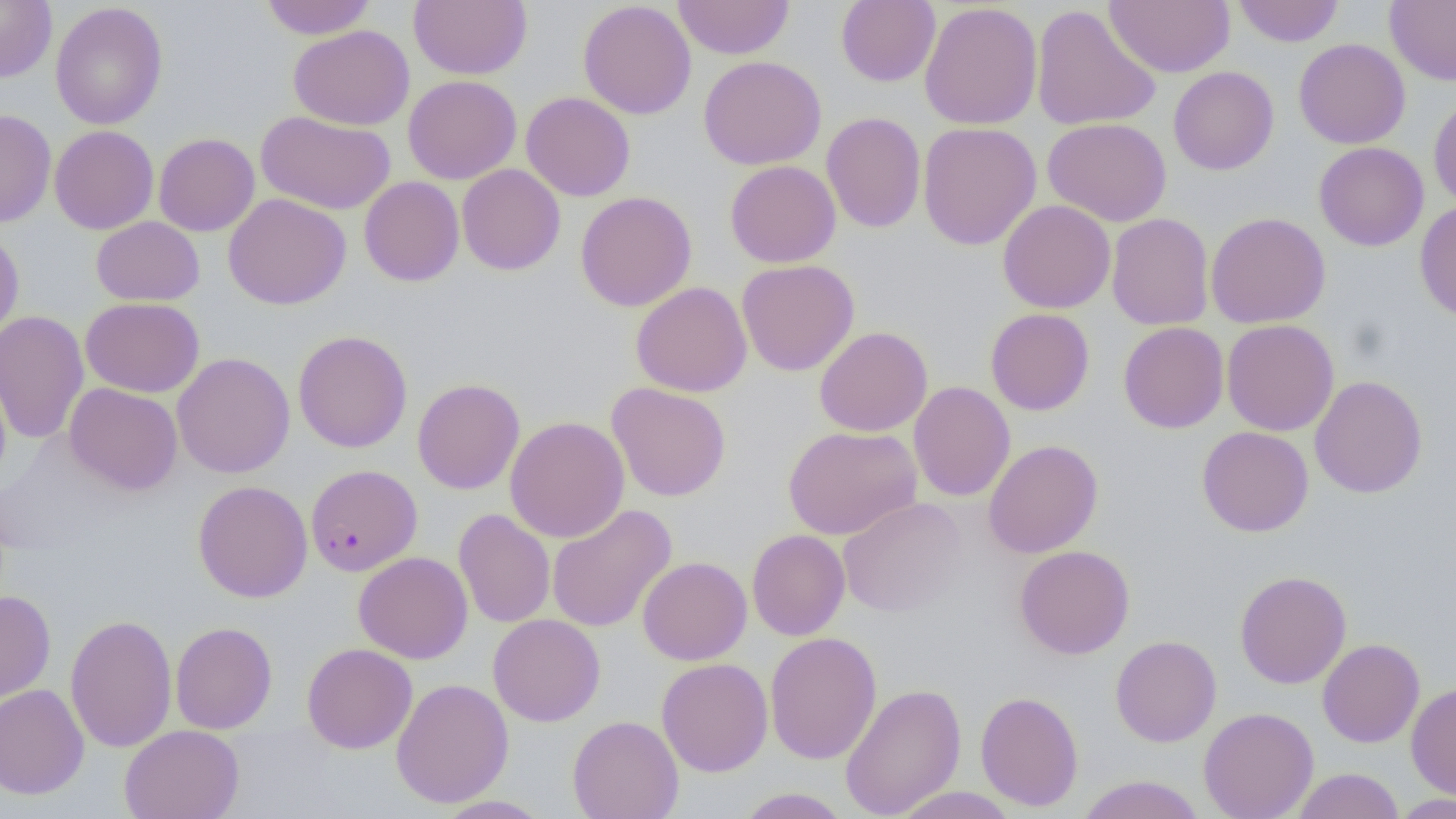
{
  "slide_level_diagnosis": "Plasmodium falciparum",
  "magnification": "1000x",
  "uninfected_red_blood_cell_locations": "approximate bounding boxes as named x1/y1/x2/y2 corners in pixels: (x1=0, y1=0, x2=56, y2=82), (x1=259, y1=0, x2=377, y2=39), (x1=409, y1=0, x2=532, y2=80), (x1=578, y1=0, x2=697, y2=119), (x1=672, y1=0, x2=794, y2=59), (x1=836, y1=0, x2=941, y2=87), (x1=1104, y1=0, x2=1234, y2=77), (x1=1233, y1=0, x2=1344, y2=47), (x1=1385, y1=0, x2=1456, y2=85), (x1=919, y1=1, x2=1042, y2=130), (x1=50, y1=2, x2=167, y2=130), (x1=1031, y1=4, x2=1161, y2=131), (x1=289, y1=25, x2=414, y2=130), (x1=1294, y1=38, x2=1410, y2=148), (x1=698, y1=55, x2=826, y2=170), (x1=1168, y1=66, x2=1279, y2=175), (x1=403, y1=75, x2=522, y2=184), (x1=521, y1=92, x2=636, y2=201), (x1=1429, y1=95, x2=1456, y2=210), (x1=0, y1=109, x2=56, y2=227), (x1=256, y1=111, x2=396, y2=214), (x1=822, y1=112, x2=925, y2=232), (x1=1043, y1=117, x2=1172, y2=226), (x1=918, y1=121, x2=1042, y2=250), (x1=50, y1=125, x2=158, y2=234), (x1=154, y1=133, x2=260, y2=236), (x1=1314, y1=142, x2=1429, y2=251), (x1=725, y1=160, x2=841, y2=268), (x1=457, y1=164, x2=565, y2=276), (x1=359, y1=176, x2=464, y2=287), (x1=575, y1=191, x2=696, y2=312), (x1=223, y1=193, x2=351, y2=309), (x1=997, y1=200, x2=1116, y2=313), (x1=1415, y1=201, x2=1456, y2=322), (x1=1107, y1=212, x2=1213, y2=331), (x1=1206, y1=212, x2=1330, y2=329), (x1=91, y1=216, x2=205, y2=306), (x1=0, y1=230, x2=24, y2=344), (x1=737, y1=259, x2=859, y2=376), (x1=630, y1=281, x2=752, y2=397), (x1=81, y1=298, x2=204, y2=397), (x1=985, y1=308, x2=1095, y2=415), (x1=0, y1=310, x2=89, y2=445), (x1=1222, y1=319, x2=1339, y2=436), (x1=1118, y1=321, x2=1229, y2=433), (x1=814, y1=326, x2=932, y2=437), (x1=292, y1=330, x2=413, y2=453), (x1=172, y1=352, x2=294, y2=478), (x1=1310, y1=375, x2=1428, y2=498), (x1=412, y1=377, x2=525, y2=495), (x1=909, y1=381, x2=1015, y2=501), (x1=606, y1=382, x2=731, y2=501), (x1=64, y1=383, x2=183, y2=495), (x1=504, y1=416, x2=630, y2=543), (x1=783, y1=425, x2=922, y2=539), (x1=1197, y1=426, x2=1313, y2=537), (x1=984, y1=439, x2=1103, y2=558), (x1=193, y1=480, x2=312, y2=603), (x1=838, y1=497, x2=968, y2=617), (x1=547, y1=504, x2=677, y2=633), (x1=453, y1=508, x2=555, y2=628), (x1=747, y1=529, x2=850, y2=640), (x1=1014, y1=545, x2=1135, y2=659), (x1=353, y1=551, x2=473, y2=663), (x1=637, y1=556, x2=752, y2=665), (x1=1235, y1=569, x2=1352, y2=689), (x1=0, y1=591, x2=56, y2=703), (x1=65, y1=613, x2=177, y2=754), (x1=488, y1=614, x2=605, y2=726), (x1=170, y1=622, x2=277, y2=734), (x1=764, y1=631, x2=882, y2=764), (x1=1110, y1=635, x2=1222, y2=747), (x1=1317, y1=638, x2=1425, y2=747), (x1=302, y1=643, x2=417, y2=753), (x1=657, y1=658, x2=773, y2=776), (x1=391, y1=677, x2=513, y2=808), (x1=840, y1=682, x2=966, y2=819), (x1=1406, y1=682, x2=1456, y2=800), (x1=0, y1=683, x2=89, y2=799), (x1=975, y1=690, x2=1084, y2=811), (x1=1198, y1=707, x2=1319, y2=819), (x1=567, y1=715, x2=684, y2=819), (x1=120, y1=724, x2=244, y2=819), (x1=1292, y1=768, x2=1404, y2=819), (x1=1075, y1=775, x2=1206, y2=819), (x1=889, y1=786, x2=1019, y2=818), (x1=734, y1=787, x2=853, y2=818), (x1=1390, y1=793, x2=1455, y2=818), (x1=433, y1=795, x2=553, y2=818)",
  "image_size": "1456×819 pixels",
  "plasmodium_falciparum_infected_red_blood_cell_locations": "approximate bounding boxes as named x1/y1/x2/y2 corners in pixels: (x1=305, y1=464, x2=422, y2=576)",
  "field_of_view": "one of a larger specimen",
  "stain": "May-Grünwald-Giemsa",
  "preparation": "thin blood film",
  "modality": "light microscopy"
}